Assess this cell for malaria.
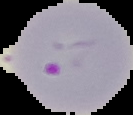
Parasitized.

image type = segmented cell region on a black background
preparation = thin blood smear
image size = 133×115 pixels